Give a bounding box for every trophozoite.
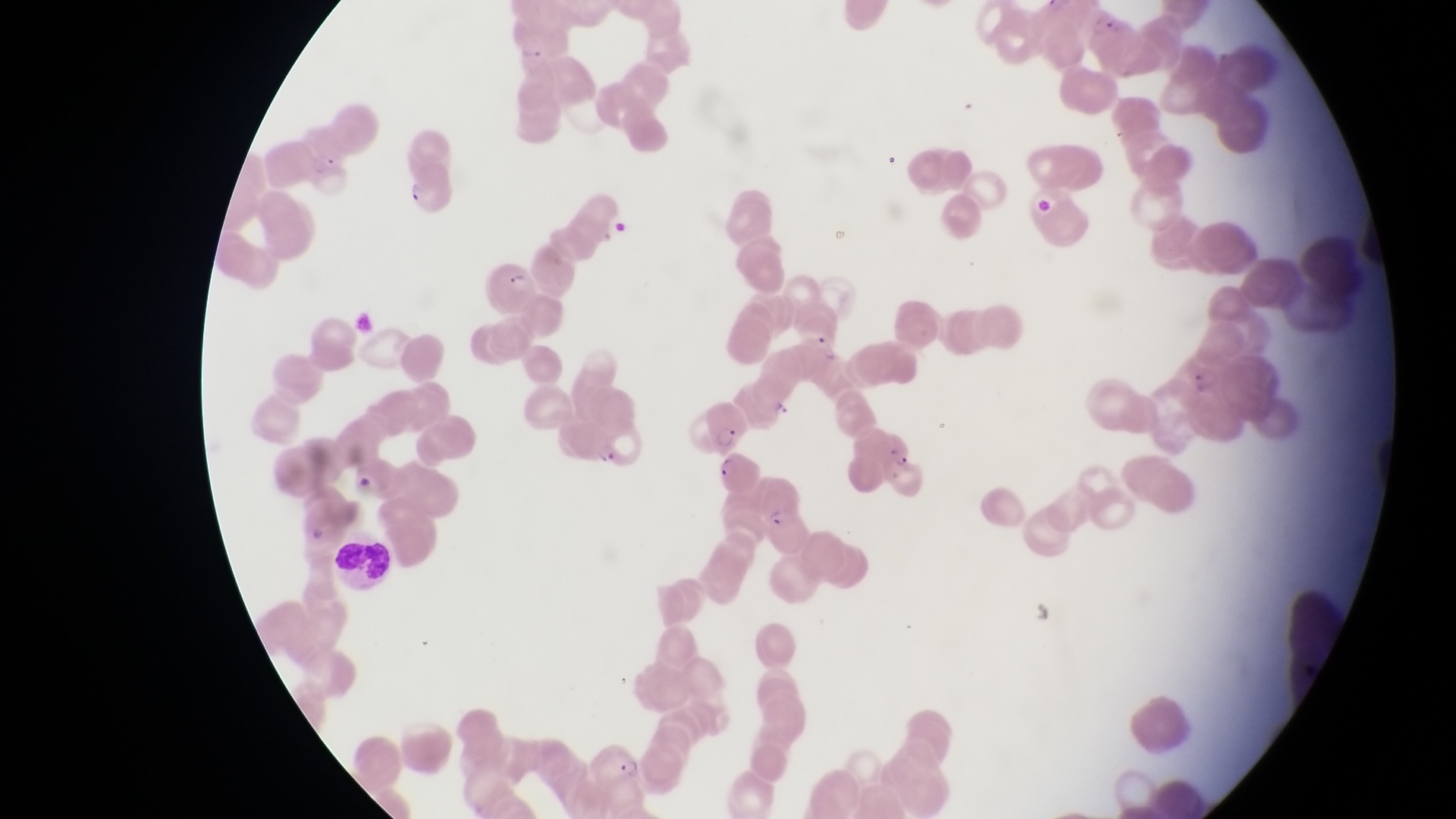

Approximate bounding boxes as (left, top, right, bottom) in pixels.
Trophozoites: (772, 403, 798, 422).

field of view = single
leukocyte locations = approximate bounding boxes as (left, top, right, bottom) in pixels: (325, 526, 396, 590)
preparation = thin blood smear
artifact (platelet-like body, stain precipitate, or debris) locations = approximate bounding boxes as (left, top, right, bottom) in pixels: (1033, 192, 1062, 218), (349, 466, 379, 493)
image size = 1456×819 pixels
parasitised red blood cell locations = approximate bounding boxes as (left, top, right, bottom) in pixels: (507, 23, 556, 63), (402, 172, 460, 215), (485, 256, 535, 309), (700, 404, 750, 451), (854, 426, 914, 476), (708, 453, 763, 496), (755, 489, 810, 552), (585, 748, 645, 793)
capture = smartphone photograph through the eyepiece of an Olympus CX-23 microscope
country = Uganda
magnification = 1000x